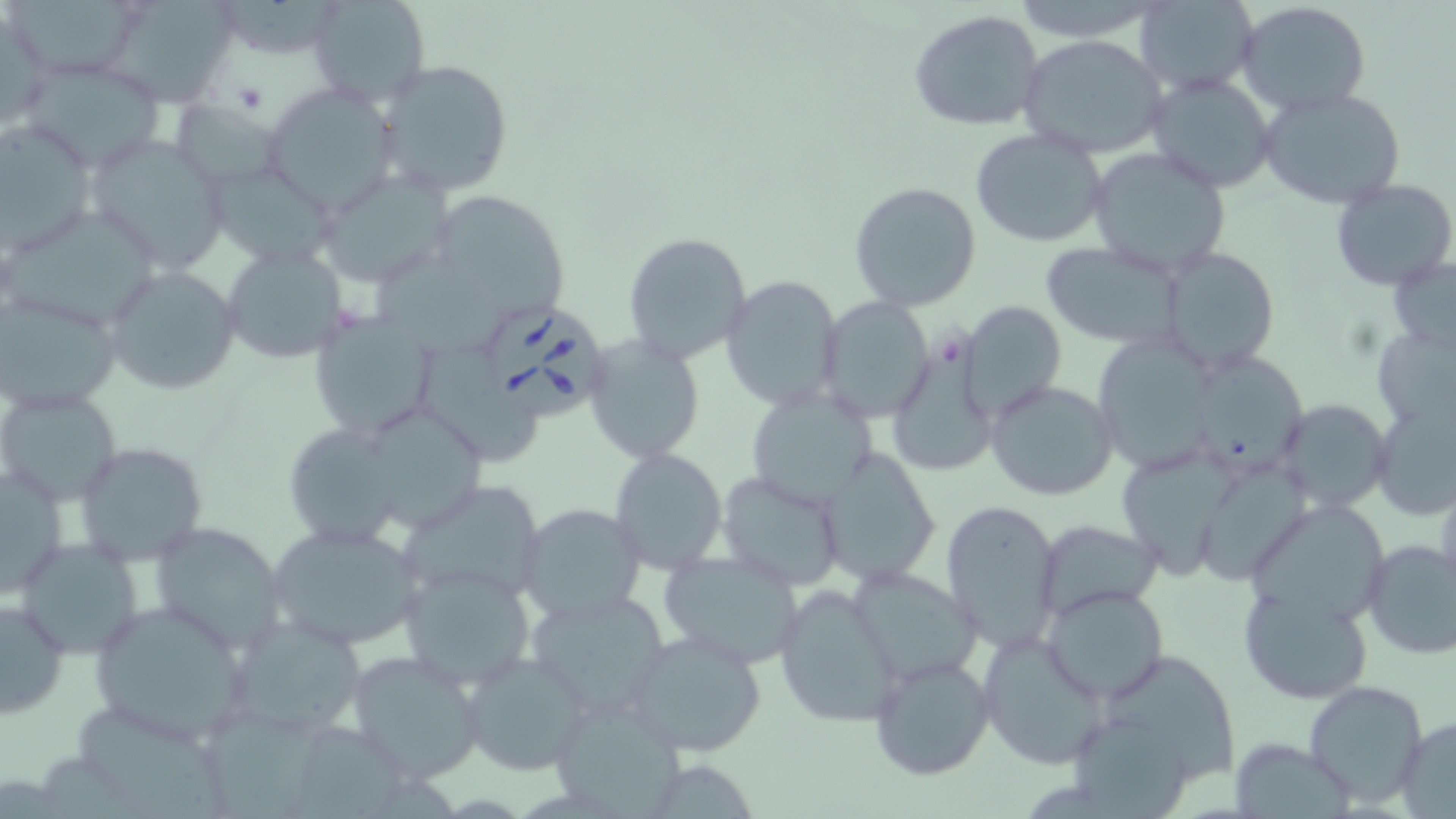 Approximate bounding boxes as named x1/y1/x2/y2 corners in pixels. Platelet locations: (x1=231, y1=83, x2=268, y2=115). Uninfected red blood cell locations: (x1=6, y1=0, x2=148, y2=81), (x1=104, y1=0, x2=235, y2=106), (x1=308, y1=0, x2=432, y2=106), (x1=1132, y1=0, x2=1260, y2=98), (x1=1235, y1=1, x2=1371, y2=116), (x1=0, y1=5, x2=54, y2=135), (x1=909, y1=11, x2=1046, y2=132), (x1=1017, y1=34, x2=1171, y2=159), (x1=21, y1=56, x2=170, y2=171), (x1=375, y1=59, x2=515, y2=199), (x1=1145, y1=73, x2=1278, y2=191), (x1=265, y1=84, x2=398, y2=210), (x1=1259, y1=88, x2=1407, y2=209), (x1=170, y1=99, x2=287, y2=188), (x1=0, y1=123, x2=100, y2=258), (x1=969, y1=127, x2=1108, y2=248), (x1=82, y1=133, x2=231, y2=273), (x1=1086, y1=145, x2=1233, y2=276), (x1=319, y1=169, x2=453, y2=290), (x1=1330, y1=178, x2=1456, y2=292), (x1=848, y1=181, x2=983, y2=312), (x1=443, y1=201, x2=570, y2=315), (x1=4, y1=206, x2=165, y2=334), (x1=622, y1=231, x2=752, y2=367), (x1=1039, y1=240, x2=1191, y2=347), (x1=220, y1=243, x2=348, y2=364), (x1=1158, y1=246, x2=1280, y2=373), (x1=370, y1=255, x2=513, y2=359), (x1=1389, y1=255, x2=1456, y2=352), (x1=103, y1=265, x2=241, y2=395), (x1=721, y1=274, x2=844, y2=411), (x1=0, y1=291, x2=122, y2=413), (x1=816, y1=296, x2=936, y2=423), (x1=956, y1=300, x2=1066, y2=422), (x1=308, y1=311, x2=437, y2=442), (x1=1371, y1=325, x2=1455, y2=431), (x1=583, y1=333, x2=705, y2=463), (x1=889, y1=336, x2=997, y2=480), (x1=1095, y1=338, x2=1213, y2=472), (x1=421, y1=347, x2=543, y2=469), (x1=1195, y1=353, x2=1316, y2=472), (x1=985, y1=380, x2=1118, y2=501), (x1=746, y1=384, x2=878, y2=508), (x1=1, y1=390, x2=124, y2=505), (x1=1274, y1=398, x2=1394, y2=513), (x1=1371, y1=401, x2=1456, y2=521), (x1=376, y1=410, x2=480, y2=534), (x1=286, y1=426, x2=407, y2=550), (x1=71, y1=442, x2=208, y2=567), (x1=609, y1=447, x2=726, y2=572), (x1=821, y1=448, x2=941, y2=584), (x1=1116, y1=453, x2=1241, y2=582), (x1=1, y1=462, x2=69, y2=599), (x1=1202, y1=467, x2=1313, y2=584), (x1=717, y1=470, x2=850, y2=591), (x1=396, y1=485, x2=547, y2=606), (x1=940, y1=497, x2=1064, y2=653), (x1=518, y1=504, x2=645, y2=625), (x1=1244, y1=507, x2=1396, y2=629), (x1=1037, y1=519, x2=1164, y2=620), (x1=152, y1=521, x2=289, y2=651), (x1=266, y1=521, x2=427, y2=651), (x1=19, y1=537, x2=145, y2=659), (x1=1361, y1=539, x2=1456, y2=662), (x1=656, y1=549, x2=809, y2=670), (x1=846, y1=564, x2=983, y2=684), (x1=396, y1=565, x2=537, y2=691), (x1=1237, y1=580, x2=1373, y2=703), (x1=774, y1=584, x2=905, y2=729), (x1=1040, y1=584, x2=1169, y2=703), (x1=525, y1=589, x2=674, y2=718), (x1=0, y1=595, x2=70, y2=717), (x1=87, y1=600, x2=254, y2=746), (x1=227, y1=613, x2=370, y2=741), (x1=621, y1=630, x2=770, y2=756), (x1=976, y1=631, x2=1109, y2=772), (x1=345, y1=649, x2=485, y2=784), (x1=460, y1=650, x2=591, y2=775), (x1=867, y1=652, x2=996, y2=781), (x1=1104, y1=657, x2=1240, y2=787), (x1=1305, y1=680, x2=1431, y2=808), (x1=547, y1=697, x2=689, y2=814), (x1=82, y1=706, x2=233, y2=819), (x1=206, y1=708, x2=325, y2=819), (x1=1073, y1=717, x2=1189, y2=819), (x1=1393, y1=719, x2=1456, y2=815), (x1=304, y1=726, x2=406, y2=819), (x1=1234, y1=743, x2=1357, y2=819). Babesia divergens-infected red blood cell locations: (x1=487, y1=308, x2=608, y2=418). Slide-level diagnosis: Babesia divergens. May-Grünwald-Giemsa stain. Thin blood film. Light microscopy. Captured at 1000x magnification. Image is 1456×819 pixels. One field of a larger specimen.